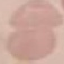
{
  "malaria_status": "uninfected",
  "preparation": "thin blood smear",
  "stain": "Giemsa",
  "capture": "smartphone through the microscope eyepiece",
  "image_type": "cell patch, automatically extracted from a larger field of view and resized to 64 × 64 pixels"
}